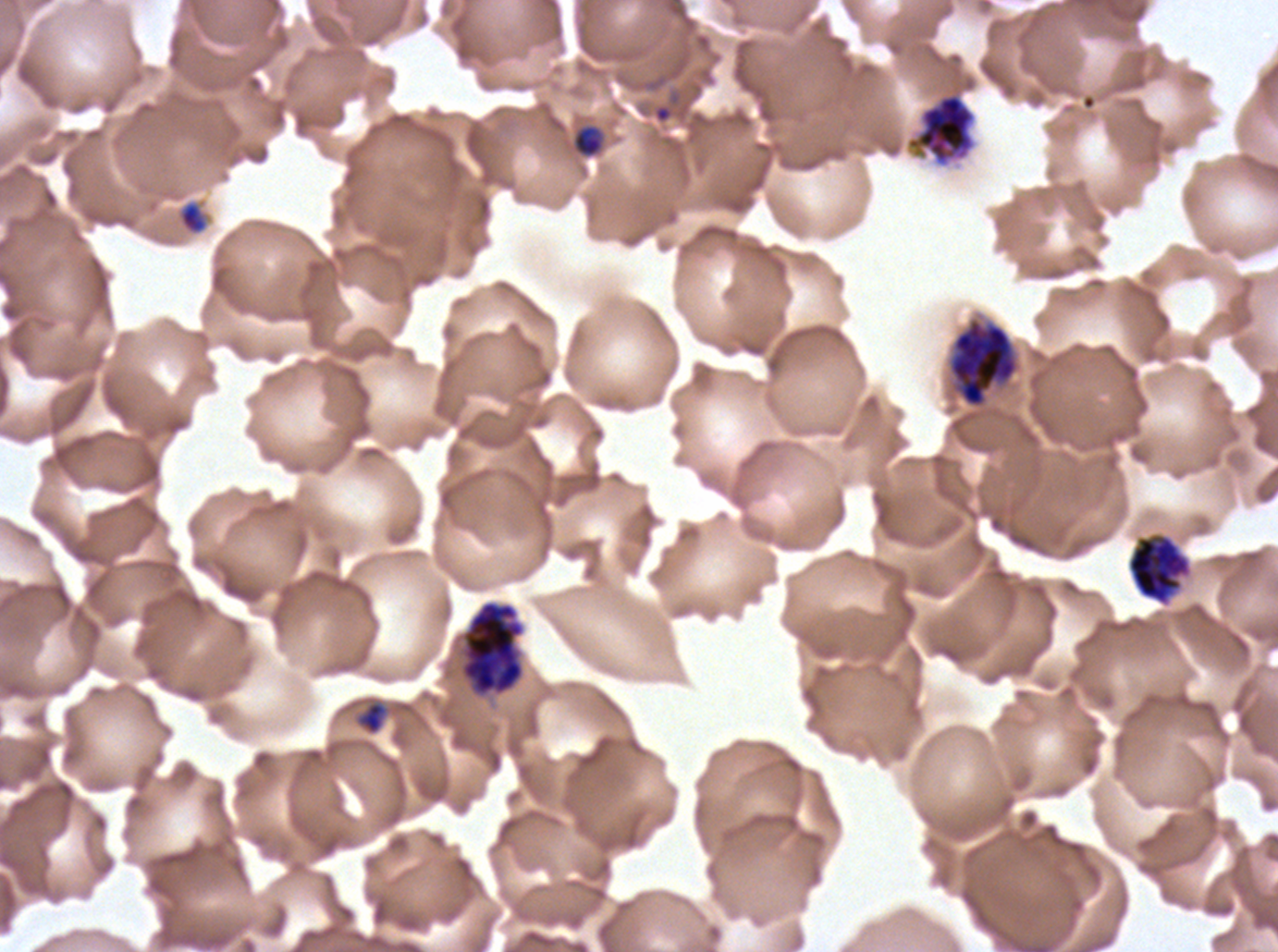 Approximate bounding boxes as [x1, y1, x2, y2] in pixels. Object labeled both ring and late-ring/early-trophozoite by the source: [571, 123, 605, 159]. Early schizont locations: [905, 92, 977, 167], [948, 318, 1019, 409], [1126, 532, 1192, 606]. Late schizont locations: [460, 600, 525, 697]. Late-ring/early-trophozoite locations: [178, 201, 209, 235], [355, 700, 388, 736]. Thin blood film. Life-cycle stages observed: late-ring/early-trophozoite, early schizont, late schizont. Plasmodium falciparum from a patient in The Gambia, cultured ex vivo for 24 to 48 hours. Image is 1278×952 pixels. One sub-image of a larger composite. Giemsa-stained preparation.